Name the blood parasite species.
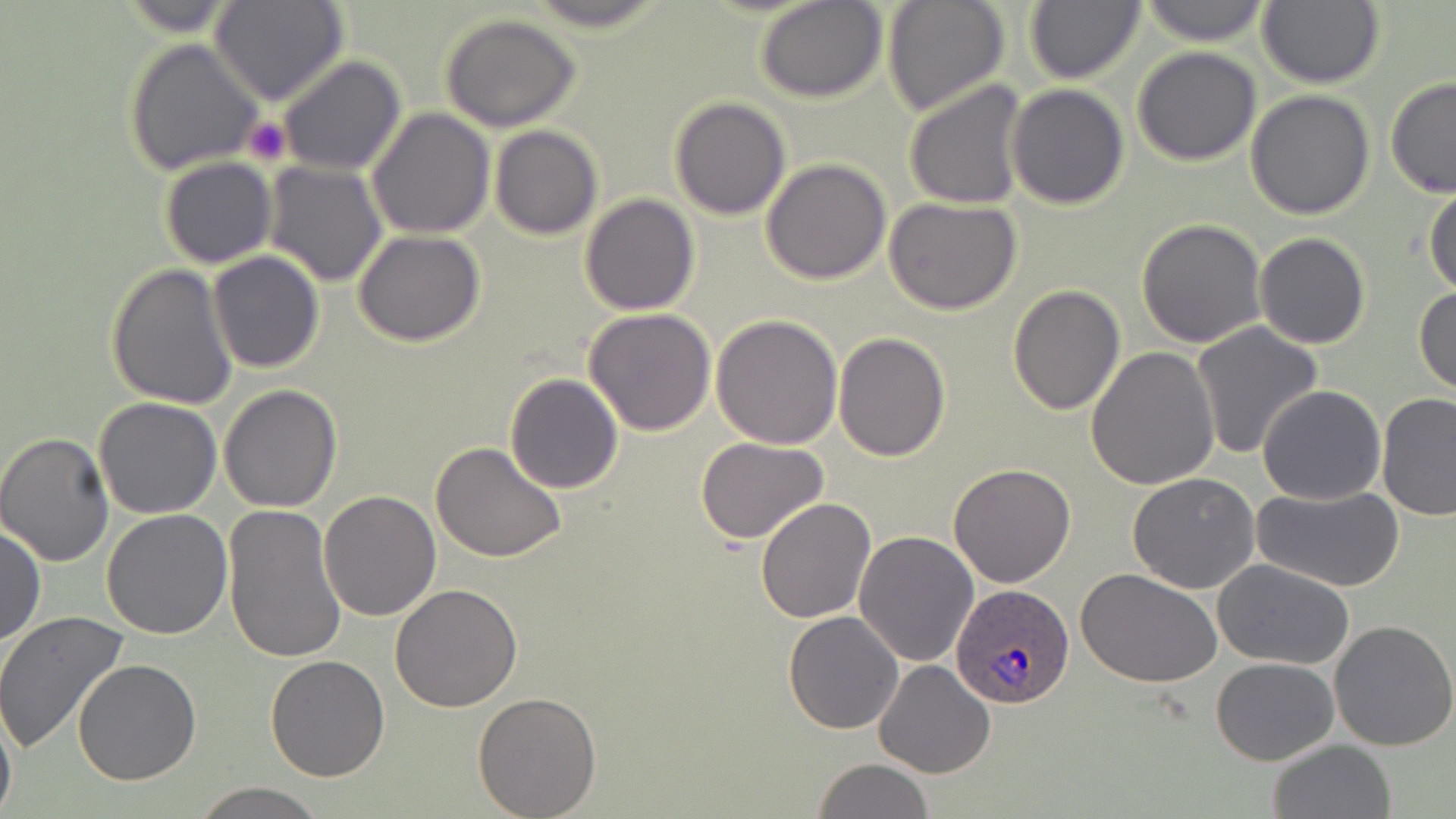
Plasmodium ovale.

Summary:
  - Coordinate format: approximate bounding boxes as named x1/y1/x2/y2 corners in pixels
  - Platelet locations: (x1=242, y1=116, x2=292, y2=167)
  - Plasmodium ovale-infected red blood cell locations: (x1=952, y1=583, x2=1075, y2=710)
  - Uninfected red blood cell locations: (x1=112, y1=0, x2=250, y2=36), (x1=882, y1=0, x2=1011, y2=117), (x1=1023, y1=0, x2=1145, y2=85), (x1=1137, y1=0, x2=1272, y2=47), (x1=1257, y1=0, x2=1384, y2=89), (x1=755, y1=1, x2=887, y2=103), (x1=210, y1=2, x2=347, y2=106), (x1=439, y1=14, x2=582, y2=132), (x1=125, y1=38, x2=261, y2=176), (x1=1131, y1=46, x2=1261, y2=166), (x1=276, y1=54, x2=405, y2=175), (x1=1384, y1=77, x2=1456, y2=198), (x1=904, y1=80, x2=1031, y2=210), (x1=1006, y1=83, x2=1130, y2=210), (x1=1245, y1=89, x2=1375, y2=219), (x1=669, y1=97, x2=792, y2=220), (x1=367, y1=107, x2=494, y2=239), (x1=490, y1=125, x2=602, y2=240), (x1=159, y1=157, x2=277, y2=268), (x1=760, y1=158, x2=890, y2=286), (x1=261, y1=160, x2=386, y2=286), (x1=1424, y1=178, x2=1456, y2=296), (x1=579, y1=192, x2=701, y2=315), (x1=883, y1=198, x2=1024, y2=316), (x1=1136, y1=218, x2=1267, y2=348), (x1=354, y1=230, x2=485, y2=347), (x1=1256, y1=233, x2=1371, y2=349), (x1=205, y1=251, x2=325, y2=374), (x1=105, y1=265, x2=238, y2=412), (x1=1006, y1=284, x2=1125, y2=415), (x1=1414, y1=286, x2=1456, y2=399), (x1=583, y1=308, x2=716, y2=436), (x1=710, y1=313, x2=843, y2=450), (x1=1192, y1=323, x2=1323, y2=458), (x1=833, y1=332, x2=952, y2=462), (x1=1086, y1=346, x2=1221, y2=490), (x1=504, y1=373, x2=625, y2=493), (x1=1258, y1=383, x2=1386, y2=505), (x1=219, y1=384, x2=342, y2=512), (x1=1377, y1=392, x2=1456, y2=523), (x1=94, y1=397, x2=222, y2=519), (x1=0, y1=431, x2=117, y2=567), (x1=695, y1=435, x2=831, y2=544), (x1=430, y1=442, x2=567, y2=563), (x1=948, y1=463, x2=1077, y2=587), (x1=1127, y1=471, x2=1261, y2=593), (x1=1254, y1=486, x2=1405, y2=593), (x1=319, y1=491, x2=440, y2=621), (x1=754, y1=497, x2=875, y2=622), (x1=223, y1=504, x2=346, y2=664), (x1=102, y1=510, x2=233, y2=641), (x1=1, y1=522, x2=45, y2=648), (x1=855, y1=529, x2=981, y2=669), (x1=1213, y1=559, x2=1356, y2=672), (x1=1076, y1=567, x2=1222, y2=687), (x1=389, y1=584, x2=522, y2=712), (x1=0, y1=611, x2=130, y2=756), (x1=784, y1=611, x2=905, y2=733), (x1=1329, y1=621, x2=1456, y2=752), (x1=264, y1=655, x2=390, y2=783), (x1=1211, y1=658, x2=1341, y2=766), (x1=73, y1=660, x2=202, y2=785), (x1=874, y1=660, x2=997, y2=779), (x1=473, y1=689, x2=603, y2=817), (x1=0, y1=699, x2=17, y2=819), (x1=1267, y1=739, x2=1398, y2=819), (x1=812, y1=758, x2=934, y2=819), (x1=192, y1=783, x2=328, y2=819)
  - Image size: 1456×819 pixels
  - Modality: light microscopy
  - Magnification: 1000x
  - Field of view: single
  - Preparation: thin blood smear
  - Stain: May-Grünwald-Giemsa